Comment on the morphology of the erythrocytes.
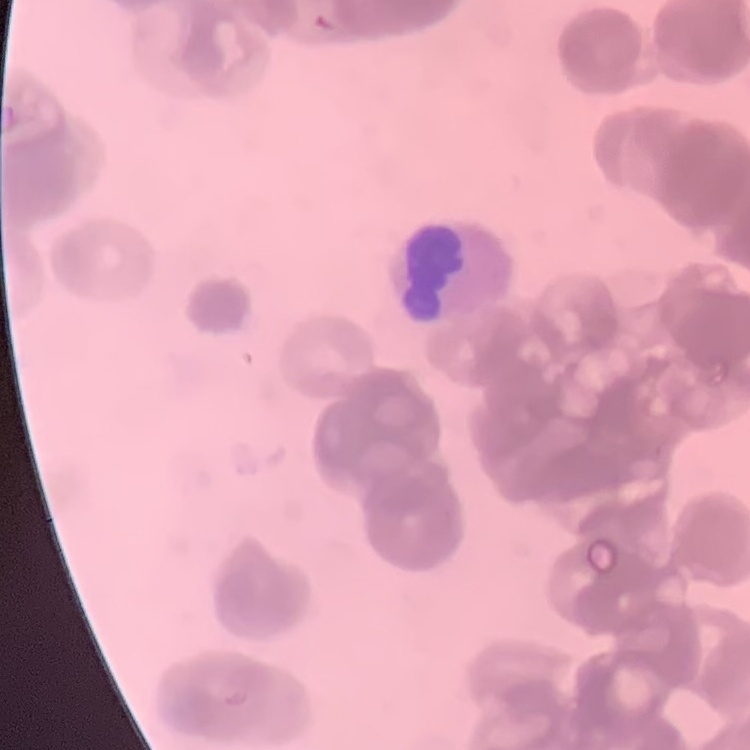

Rouleaux formation.

preparation = thin blood film
stain = Field's or Giemsa
image type = square crop of a larger photomicrograph